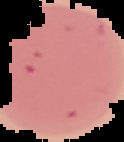
result = no Plasmodium parasites detected
image type = cell region segmented out of the field of view; surrounding area masked to black
preparation = thin blood film
image size = 124×142 pixels